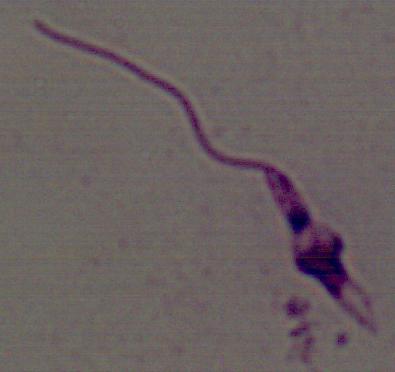

{
  "magnification": "1000x",
  "modality": "micrograph",
  "identification": "Leishmania"
}